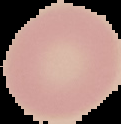

Summary:
  - Image type: segmented cell region on a black background
  - Preparation: thin blood smear
  - Malaria status: uninfected
  - Image size: 121×124 pixels